Name the parasite shown.
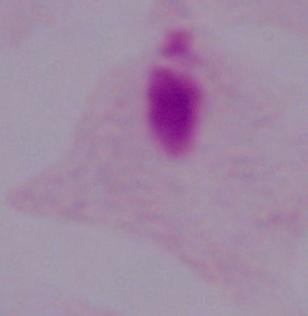

This is a trichomonad.

1000x magnification. Photomicrograph.